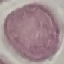
Summary:
  - Result: no malaria parasites seen
  - Preparation: thin blood smear
  - Capture: smartphone through the microscope eyepiece
  - Stain: Giemsa
  - Image type: cell patch, automatically extracted from a larger field of view and resized to 64 × 64 pixels